Point out each leukocyte.
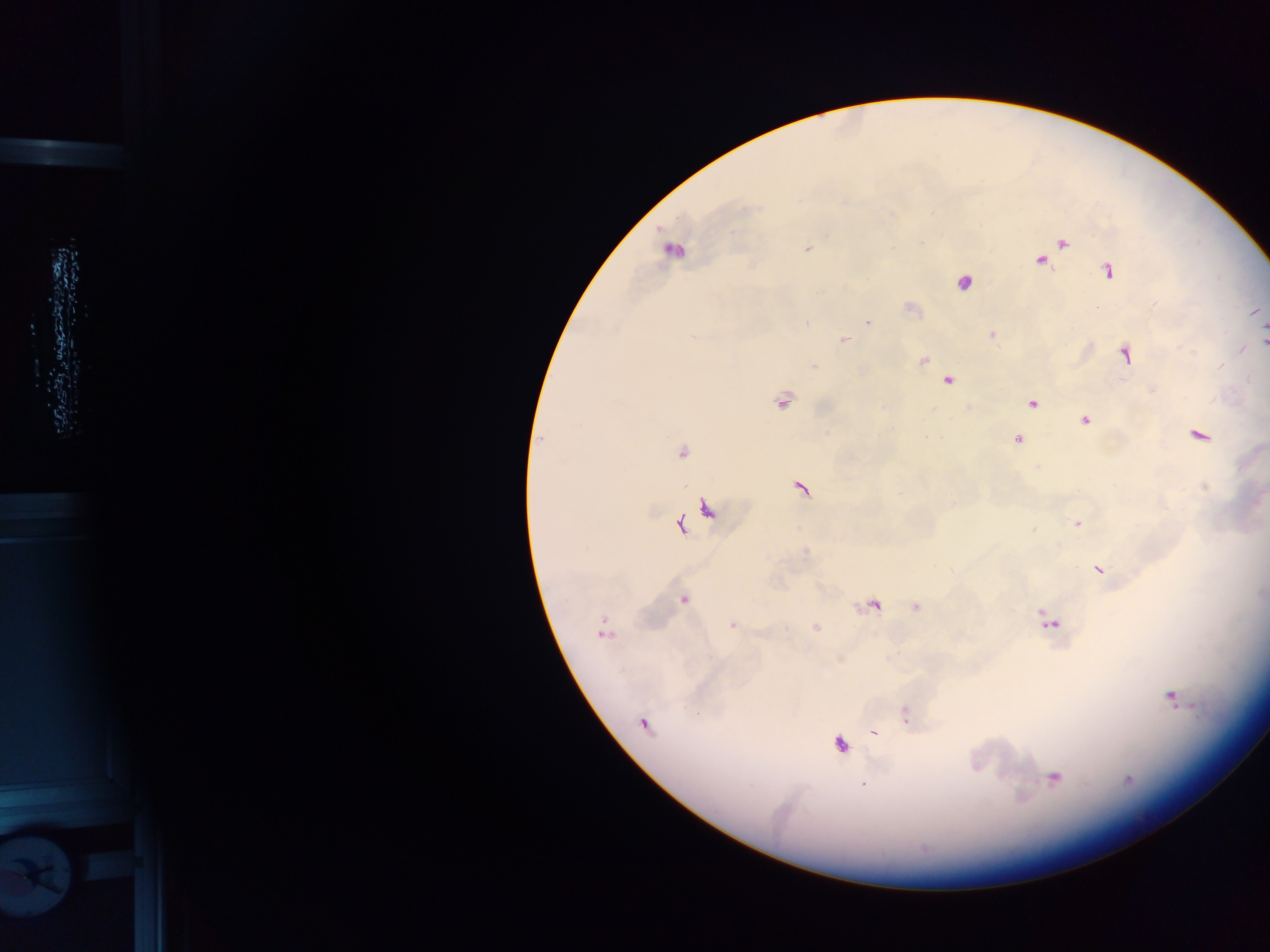

No leukocytes observed.

Approximate centers as (x, y) in pixels. Plasmodium parasite locations: (1062, 242), (806, 248), (672, 249), (1042, 259), (1108, 270), (963, 282), (909, 307), (867, 322), (992, 335), (693, 337), (843, 340), (1264, 340), (1126, 354), (922, 359), (813, 366), (862, 371), (946, 379), (1153, 389), (783, 400), (1031, 402), (1084, 419), (1198, 434), (1017, 439), (681, 452), (801, 487), (709, 509), (1076, 522), (679, 525), (804, 552), (1099, 568), (684, 599), (872, 604), (915, 606), (1048, 620), (732, 624), (815, 627), (602, 630), (1170, 696), (906, 716), (643, 724), (874, 732), (838, 743), (1053, 777), (862, 784). Image is 1270×952 pixels. Photographed through a microscope with a mobile-phone camera. Thick blood smear. Sample from Ghana. One field of view.